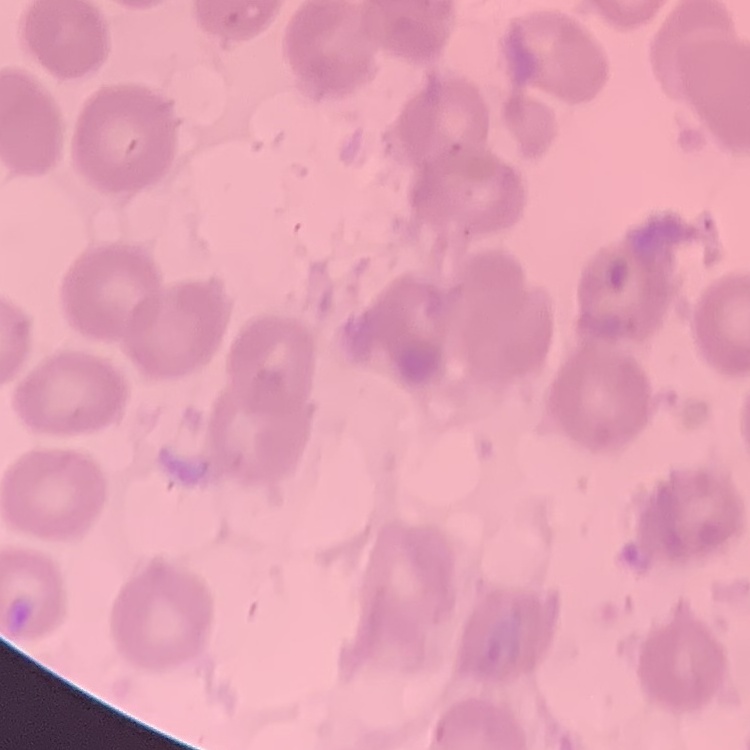
The red blood cells exhibit no rouleaux formation. Thin peripheral smear. Square crop of a larger photomicrograph. Stained with either Field's or Giemsa.